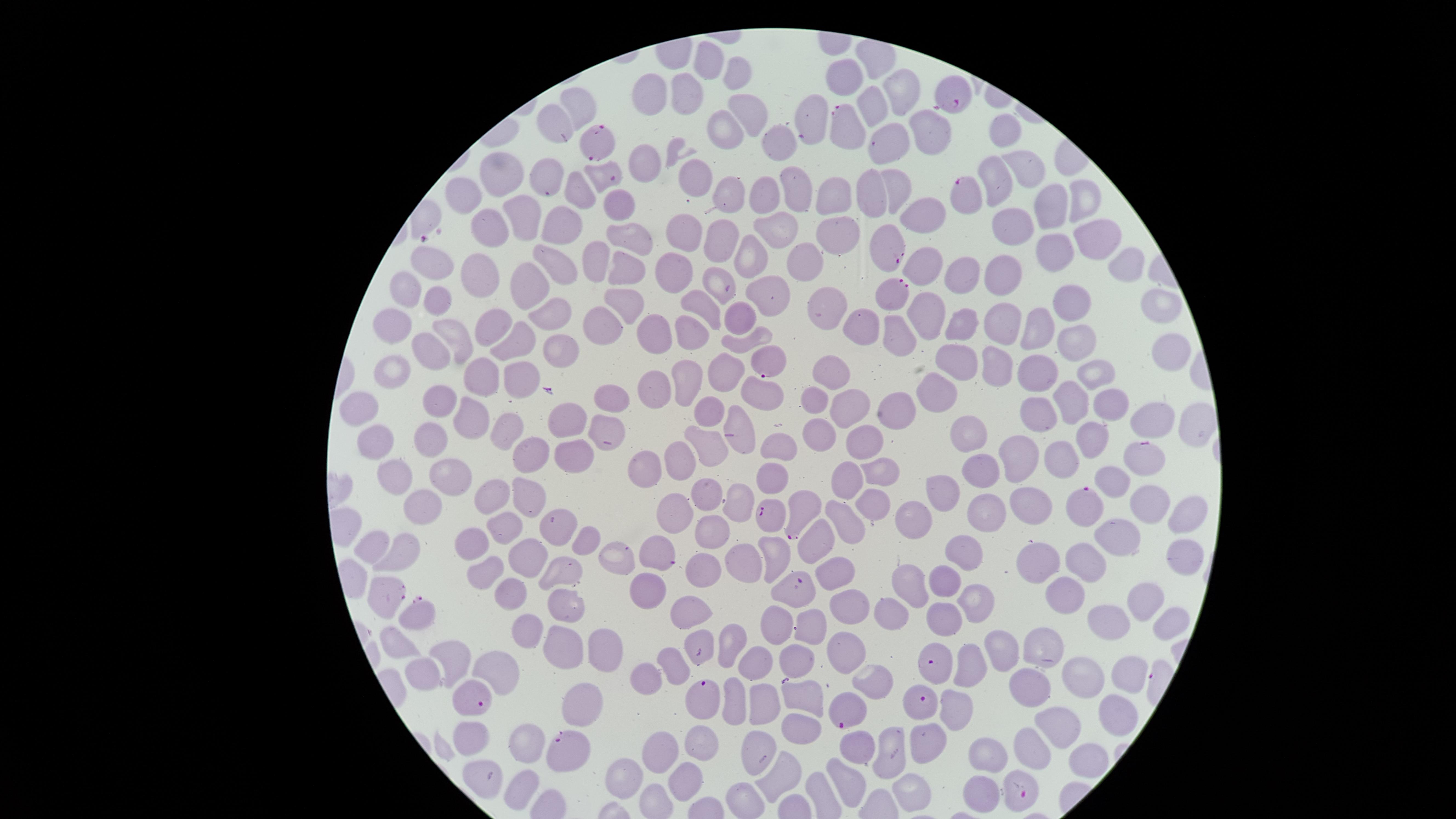 Approximate marker points, in pixels from the top-left corner. Parasitized RBCs: (x=950, y=96), (x=842, y=129), (x=596, y=137), (x=606, y=177), (x=966, y=193), (x=885, y=248), (x=899, y=295), (x=764, y=361), (x=1138, y=456), (x=1083, y=505), (x=800, y=513), (x=771, y=515), (x=657, y=554), (x=384, y=590), (x=799, y=591), (x=417, y=617), (x=935, y=659), (x=704, y=700), (x=473, y=701), (x=921, y=703), (x=847, y=713), (x=568, y=749), (x=1026, y=791). Uninfected RBCs: (x=716, y=61), (x=742, y=74), (x=853, y=75), (x=649, y=91), (x=903, y=92), (x=692, y=94), (x=874, y=106), (x=750, y=107), (x=573, y=109), (x=809, y=117), (x=558, y=123), (x=722, y=130), (x=929, y=133), (x=1007, y=133), (x=776, y=145), (x=891, y=145), (x=653, y=155), (x=546, y=166), (x=1023, y=168), (x=500, y=175), (x=695, y=177), (x=997, y=178), (x=893, y=190), (x=571, y=191), (x=793, y=191), (x=868, y=191), (x=765, y=193), (x=720, y=194), (x=829, y=194), (x=1082, y=198), (x=468, y=201), (x=1049, y=203), (x=615, y=208), (x=921, y=211), (x=523, y=216), (x=1014, y=223), (x=775, y=228), (x=493, y=229), (x=558, y=231), (x=675, y=232), (x=833, y=232), (x=628, y=235), (x=718, y=238), (x=1089, y=239), (x=1053, y=243), (x=751, y=254), (x=809, y=261), (x=593, y=264), (x=920, y=265), (x=435, y=267), (x=622, y=267), (x=1116, y=269), (x=553, y=270), (x=965, y=270), (x=999, y=273), (x=475, y=274), (x=671, y=279), (x=718, y=283), (x=523, y=288), (x=765, y=288), (x=407, y=292), (x=1152, y=302), (x=441, y=303), (x=623, y=303), (x=826, y=303), (x=1069, y=304), (x=706, y=306), (x=545, y=311), (x=922, y=315), (x=1006, y=318), (x=737, y=321), (x=399, y=325), (x=599, y=325), (x=654, y=325), (x=692, y=325), (x=857, y=326), (x=963, y=326), (x=1032, y=326), (x=494, y=329), (x=896, y=332), (x=459, y=339), (x=522, y=340), (x=1078, y=343), (x=740, y=345), (x=433, y=350), (x=562, y=350), (x=1169, y=350), (x=954, y=360), (x=999, y=363), (x=400, y=369), (x=722, y=370), (x=834, y=370), (x=489, y=371), (x=1041, y=372), (x=1096, y=373), (x=518, y=377), (x=680, y=381), (x=651, y=382), (x=763, y=393), (x=932, y=395), (x=439, y=396), (x=609, y=396), (x=810, y=399), (x=1073, y=400), (x=896, y=404), (x=361, y=405), (x=841, y=408), (x=1109, y=408), (x=709, y=412), (x=1034, y=414), (x=1148, y=415), (x=474, y=417), (x=735, y=417), (x=566, y=420), (x=599, y=426), (x=1192, y=428), (x=970, y=432), (x=507, y=433), (x=818, y=433), (x=429, y=435), (x=1092, y=435), (x=861, y=439), (x=373, y=442), (x=778, y=442), (x=708, y=445), (x=679, y=453), (x=1019, y=453), (x=528, y=454), (x=571, y=457), (x=1063, y=458), (x=641, y=466), (x=878, y=469), (x=981, y=471), (x=843, y=475), (x=447, y=476), (x=1114, y=477), (x=773, y=479), (x=393, y=484), (x=940, y=492), (x=708, y=495), (x=497, y=497), (x=740, y=502), (x=881, y=502), (x=1034, y=503), (x=527, y=506), (x=1143, y=506), (x=992, y=510), (x=919, y=513), (x=424, y=514), (x=677, y=517), (x=850, y=519), (x=1180, y=519), (x=504, y=526), (x=555, y=526), (x=714, y=533), (x=1120, y=534), (x=826, y=540), (x=586, y=542), (x=476, y=543), (x=374, y=547), (x=966, y=548), (x=1181, y=552), (x=525, y=553), (x=401, y=554), (x=773, y=554), (x=745, y=559), (x=616, y=560), (x=1045, y=560), (x=1082, y=560), (x=562, y=568), (x=487, y=573), (x=705, y=574), (x=838, y=574), (x=946, y=580), (x=900, y=583), (x=509, y=591), (x=652, y=592), (x=1070, y=597), (x=1139, y=600), (x=970, y=603), (x=563, y=605), (x=850, y=608), (x=693, y=609), (x=887, y=615), (x=941, y=616), (x=1107, y=622), (x=1161, y=624), (x=810, y=628), (x=526, y=637), (x=699, y=640), (x=730, y=640), (x=397, y=644), (x=605, y=647), (x=1003, y=647), (x=1050, y=647), (x=564, y=650), (x=838, y=653), (x=754, y=657), (x=799, y=657), (x=455, y=665), (x=970, y=666), (x=675, y=667), (x=1131, y=673), (x=426, y=675), (x=1085, y=675), (x=492, y=677), (x=1034, y=678), (x=655, y=680), (x=880, y=682), (x=732, y=700), (x=801, y=701), (x=768, y=702), (x=583, y=703), (x=957, y=708), (x=1109, y=715), (x=803, y=722), (x=1057, y=727), (x=468, y=738), (x=934, y=741), (x=533, y=742), (x=705, y=742), (x=1031, y=745), (x=900, y=747), (x=857, y=748), (x=761, y=750), (x=665, y=752), (x=990, y=755), (x=1086, y=758), (x=782, y=774), (x=481, y=779), (x=635, y=781), (x=689, y=781), (x=522, y=785), (x=846, y=791), (x=903, y=792), (x=981, y=792). Thin blood film. Species: Plasmodium falciparum. Photographed with a smartphone camera through the microscope eyepiece. Image is 1456×819 pixels. Giemsa-stained preparation. One field of view of the specimen. Circular visible region. Presence: malaria parasites detected.